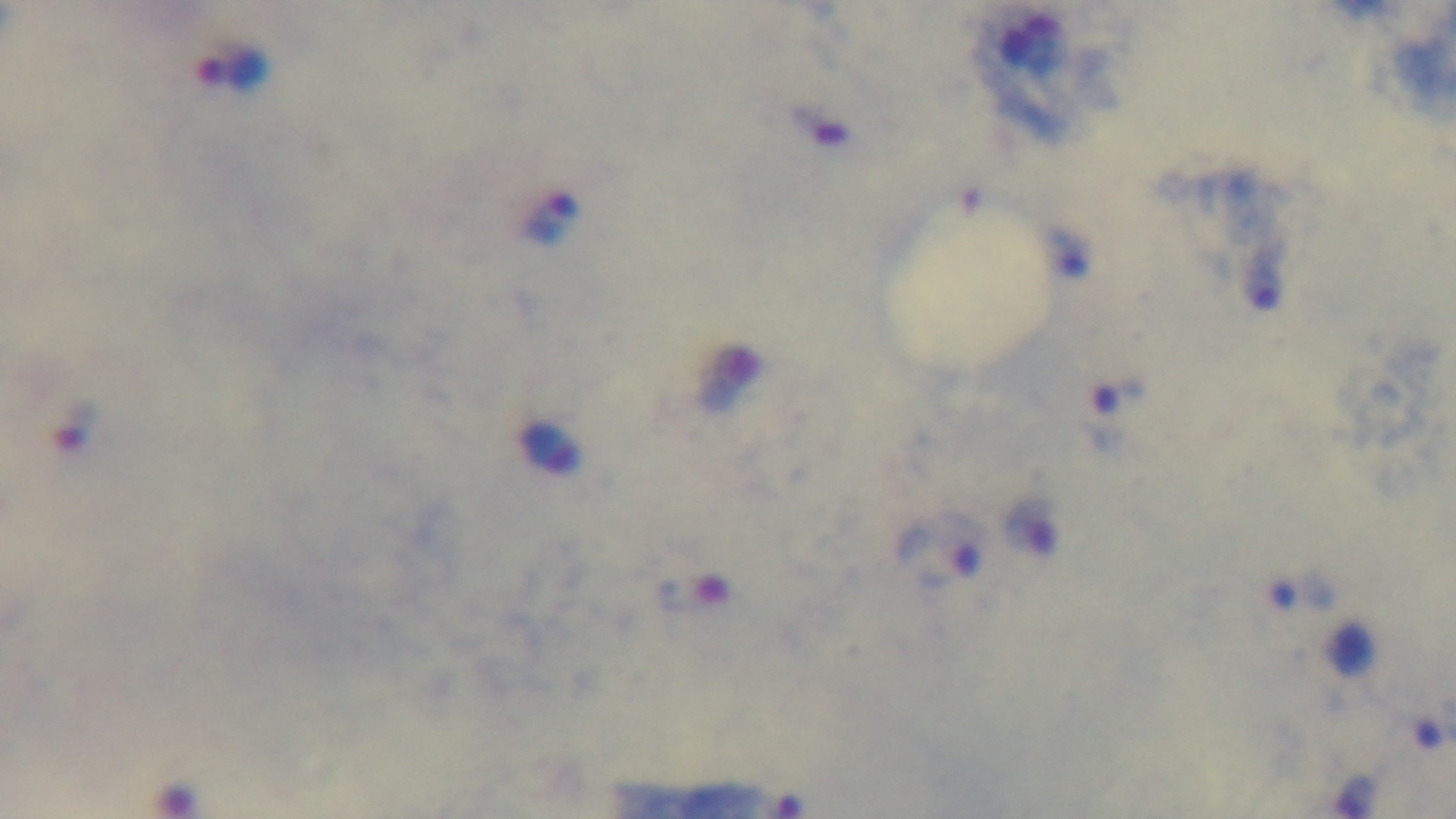 Malaria status: positive. Captured with a mounted 4K digital camera. Single field of view. 100x oil-immersion objective. Giemsa stain. Preparation: thick smear. Photomicrograph.